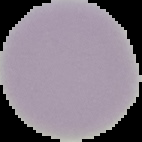 From a thin blood smear. Result: negative for malaria parasites. Image is 142×142 pixels. The area outside the segmented cell region is set to black.